Name the cell type shown.
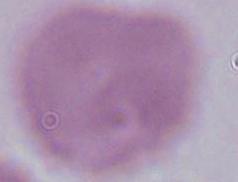

This is an erythrocyte.

{
  "modality": "micrograph",
  "magnification": "1000x"
}